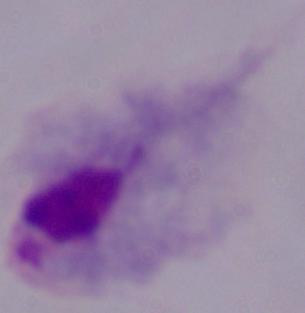
Summary:
  - Modality: micrograph
  - Magnification: 1000x
  - Identification: trichomonad